Point out each Plasmodium parasite.
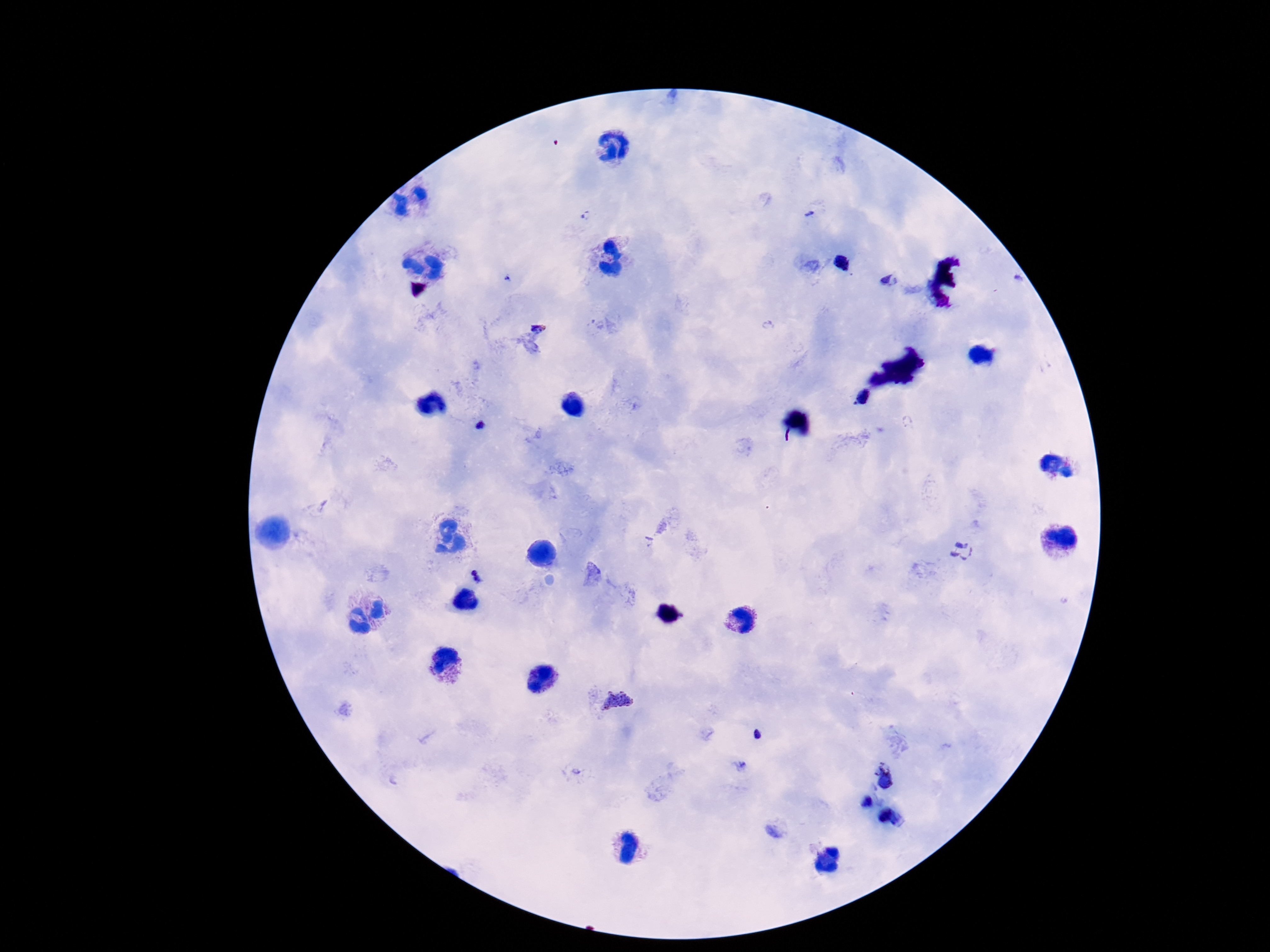

Approximate centers as [x, y] in pixels.
Plasmodium parasites: [841, 263], [891, 281], [538, 324], [861, 396], [479, 426], [963, 549], [480, 574], [621, 702], [758, 734], [886, 773], [866, 802], [892, 815].

Summary:
  - Patient malaria status: positive
  - Preparation: thick peripheral-blood smear
  - Magnification: 100x
  - Stain: Giemsa
  - Image size: 1270×952 pixels
  - Capture: smartphone camera through the microscope eyepiece
  - Field of view: one from this slide